State the preparation type.
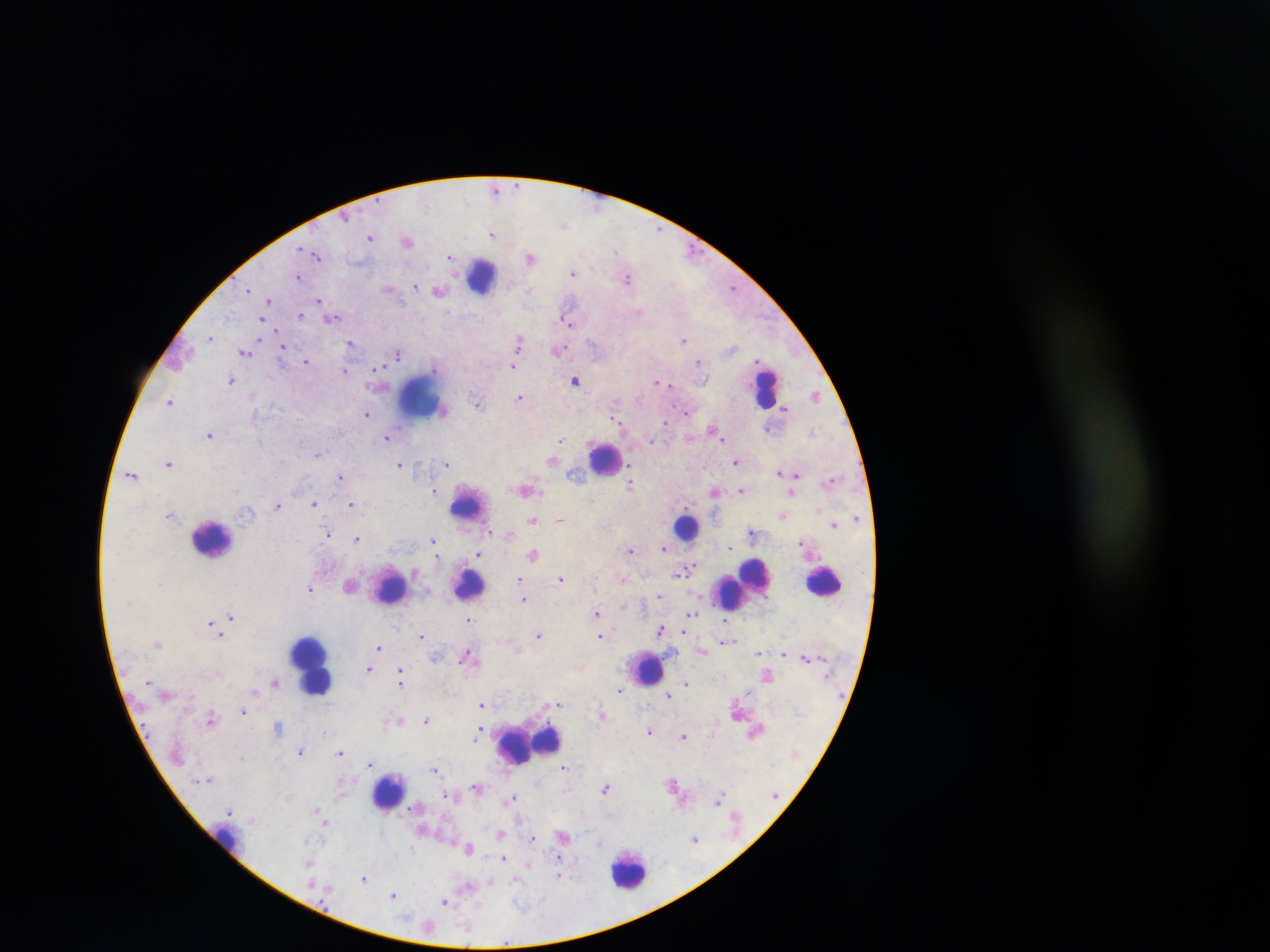

Thick blood smear.

Approximate centers as {x, y} in pixels.
Summary:
  - Leukocyte locations: {484, 275}, {767, 387}, {421, 398}, {607, 457}, {468, 504}, {687, 527}, {213, 538}, {825, 581}, {468, 584}, {742, 585}, {389, 586}, {313, 663}, {646, 668}, {530, 741}, {388, 792}, {228, 839}, {629, 869}
  - Malaria parasite locations: {496, 188}, {466, 201}, {565, 224}, {493, 233}, {371, 238}, {408, 241}, {616, 250}, {317, 254}, {450, 256}, {530, 257}, {574, 272}, {298, 276}, {629, 278}, {415, 285}, {734, 287}, {389, 288}, {529, 289}, {248, 290}, {440, 290}, {319, 299}, {268, 300}, {640, 312}, {300, 314}, {332, 317}, {568, 319}, {265, 323}, {211, 336}, {262, 338}, {684, 339}, {519, 341}, {351, 342}, {283, 346}, {245, 350}, {559, 350}, {399, 353}, {699, 360}, {306, 361}, {514, 365}, {378, 367}, {344, 370}, {232, 380}, {576, 380}, {657, 381}, {668, 382}, {253, 393}, {816, 395}, {520, 396}, {170, 401}, {478, 403}, {444, 408}, {786, 408}, {688, 412}, {368, 413}, {614, 417}, {665, 422}, {768, 428}, {713, 429}, {813, 431}, {210, 433}, {387, 437}, {561, 438}, {651, 441}, {318, 453}, {553, 460}, {170, 462}, {736, 462}, {401, 463}, {447, 463}, {781, 471}, {796, 472}, {132, 474}, {340, 476}, {630, 484}, {525, 489}, {742, 489}, {435, 490}, {715, 491}, {792, 492}, {590, 498}, {314, 503}, {351, 504}, {278, 505}, {170, 515}, {782, 515}, {533, 519}, {560, 519}, {835, 525}, {490, 531}, {751, 532}, {330, 534}, {357, 538}, {434, 541}, {731, 546}, {665, 549}, {631, 550}, {479, 553}, {438, 554}, {534, 555}, {681, 573}, {562, 577}, {520, 578}, {622, 579}, {350, 584}, {311, 589}, {661, 596}, {524, 599}, {598, 613}, {690, 615}, {230, 616}, {469, 618}, {726, 621}, {212, 624}, {661, 629}, {219, 631}, {686, 631}, {421, 635}, {538, 635}, {601, 636}, {726, 641}, {158, 645}, {379, 647}, {702, 651}, {758, 653}, {783, 653}, {468, 656}, {806, 657}, {435, 658}, {369, 669}, {402, 675}, {767, 675}, {275, 682}, {686, 683}, {400, 687}, {620, 690}, {257, 692}, {669, 695}, {482, 703}, {560, 703}, {244, 710}, {603, 716}, {211, 719}, {401, 719}, {426, 720}, {280, 726}, {481, 728}, {650, 731}, {712, 733}, {684, 735}, {475, 738}, {301, 751}, {340, 752}, {370, 764}, {563, 766}, {435, 769}, {339, 782}, {673, 783}, {477, 786}, {606, 788}, {452, 795}, {289, 796}, {513, 797}, {720, 800}, {316, 808}, {230, 812}, {319, 813}, {325, 821}, {501, 834}, {564, 836}, {534, 838}, {695, 838}, {600, 842}, {470, 848}, {504, 858}, {308, 862}, {528, 863}, {560, 876}, {364, 878}, {517, 879}, {490, 881}, {469, 886}, {394, 895}, {445, 900}
  - Country: Ghana
  - Image size: 1270×952 pixels
  - Capture: mobile-phone photograph through a microscope
  - Field of view: single